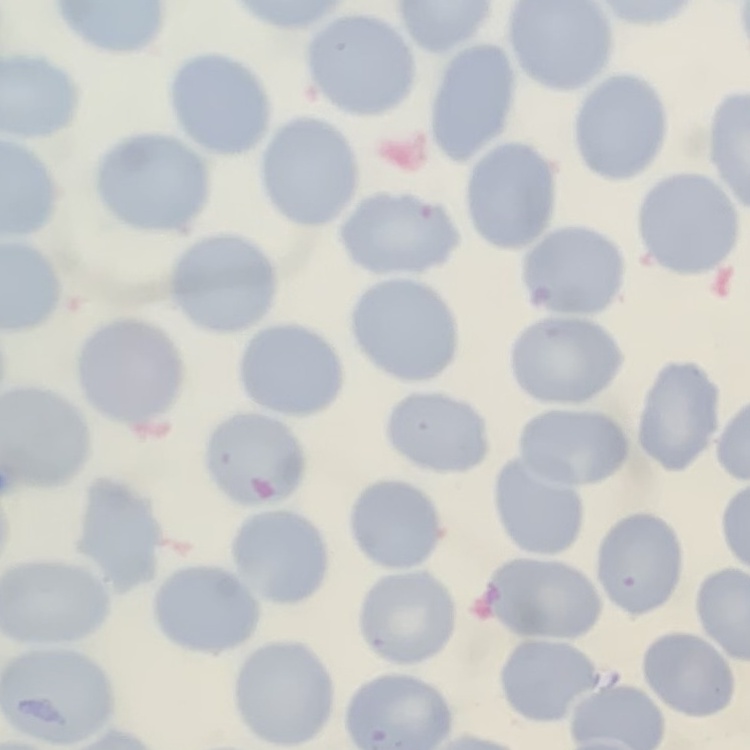 The erythrocytes show no rouleaux formation. Thin peripheral smear. Field's or Giemsa stain. One tile cut from a larger photomicrograph.